Name the cell type shown.
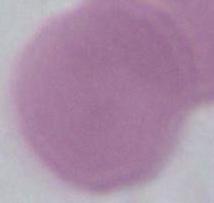
An erythrocyte.

Captured at 1000x magnification. Micrograph.